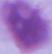

Summary:
  - Magnification: 1000x
  - Modality: micrograph
  - Identification: erythrocyte